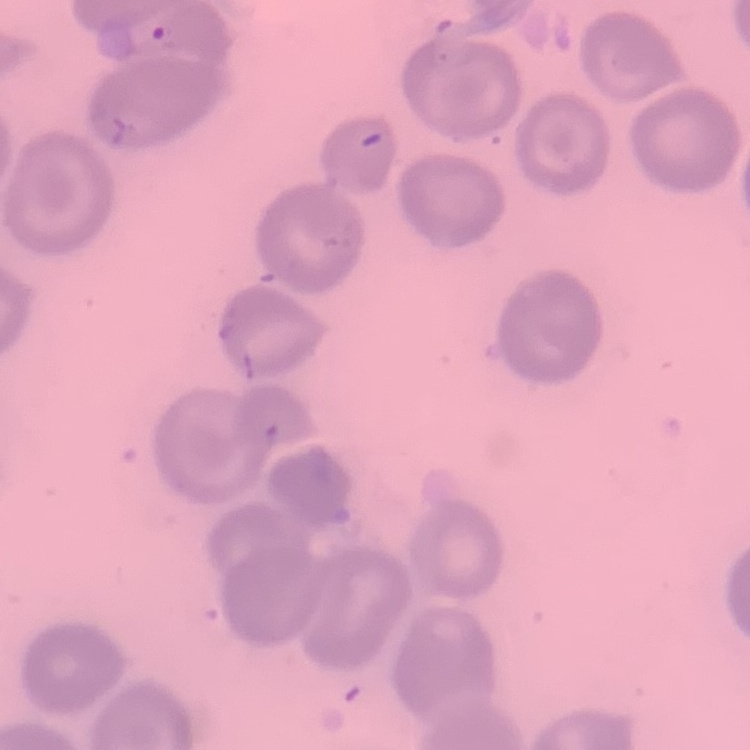

Summary:
  - Erythrocyte morphology: no rouleaux formation
  - Preparation: thin peripheral smear
  - Stain: Field's or Giemsa
  - Image type: square crop of a larger photomicrograph